Assess this cell for malaria.
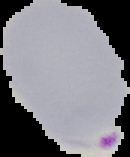

It is parasitized.

preparation = thin blood smear
image size = 130×157 pixels
image type = cell region segmented out of the field of view; surrounding area masked to black